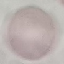
Summary:
  - Result: no malaria parasites detected
  - Capture: smartphone through the microscope eyepiece
  - Image type: automatically extracted cell patch, resized to 64 × 64 pixels
  - Stain: Giemsa
  - Preparation: thin smear